Comment on the morphology of the erythrocytes.
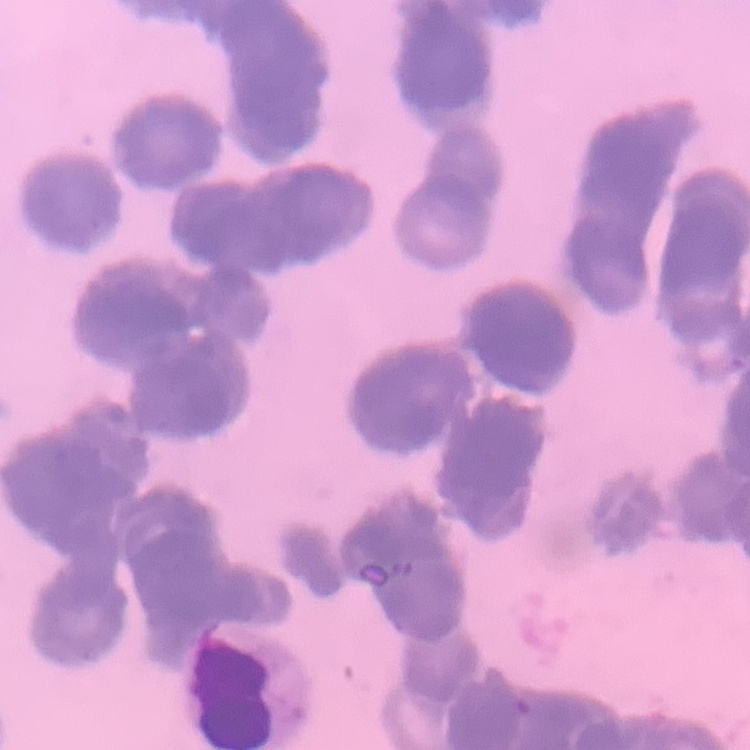

Rouleaux formation.

Stained with either Field's or Giemsa. Square crop of a larger photomicrograph. Thin blood film.